Classify this cell by malaria status.
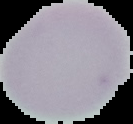

It is uninfected.

preparation = thin blood film
image type = segmented cell region with the area outside set to black
image size = 133×124 pixels